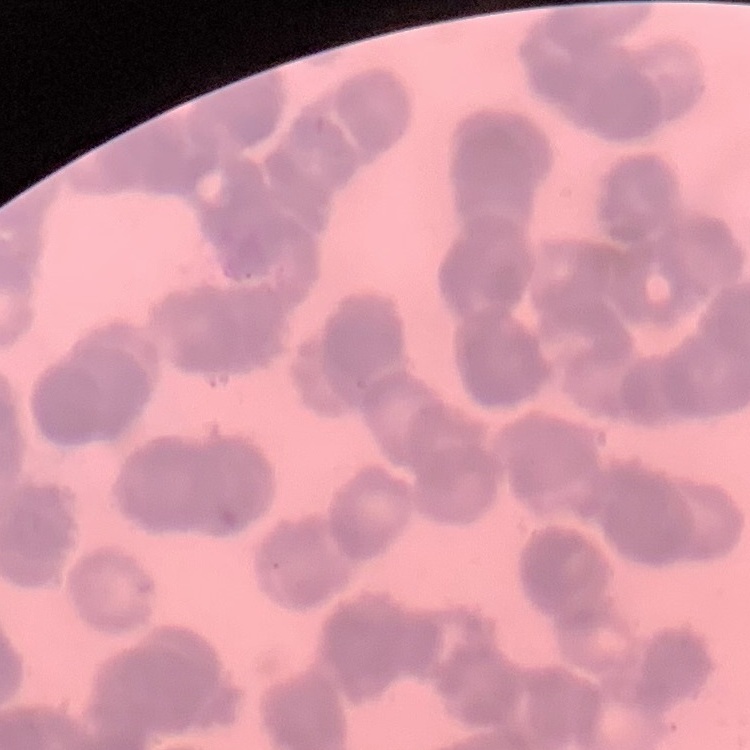
Summary:
  - Red blood cell morphology: rouleaux formation
  - Image type: square crop of a larger photomicrograph
  - Preparation: thin blood smear
  - Stain: Field's or Giemsa